Report the malaria status of this cell.
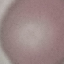
It is uninfected.

Summary:
  - Image type: cell patch, automatically extracted from a larger field of view and resized to 64 × 64 pixels
  - Capture: smartphone camera at the microscope eyepiece
  - Preparation: thin blood smear
  - Stain: Giemsa